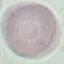

Summary:
  - Result: negative for malaria parasites
  - Stain: Giemsa
  - Preparation: thin blood film
  - Capture: smartphone camera at the microscope eyepiece
  - Image type: automatically extracted cell patch, resized to 64 × 64 pixels